Identify the parasite.
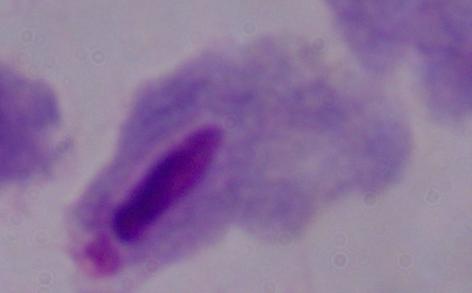

This is a trichomonad.

{
  "modality": "micrograph",
  "magnification": "1000x"
}